Locate and identify every blood parasite.
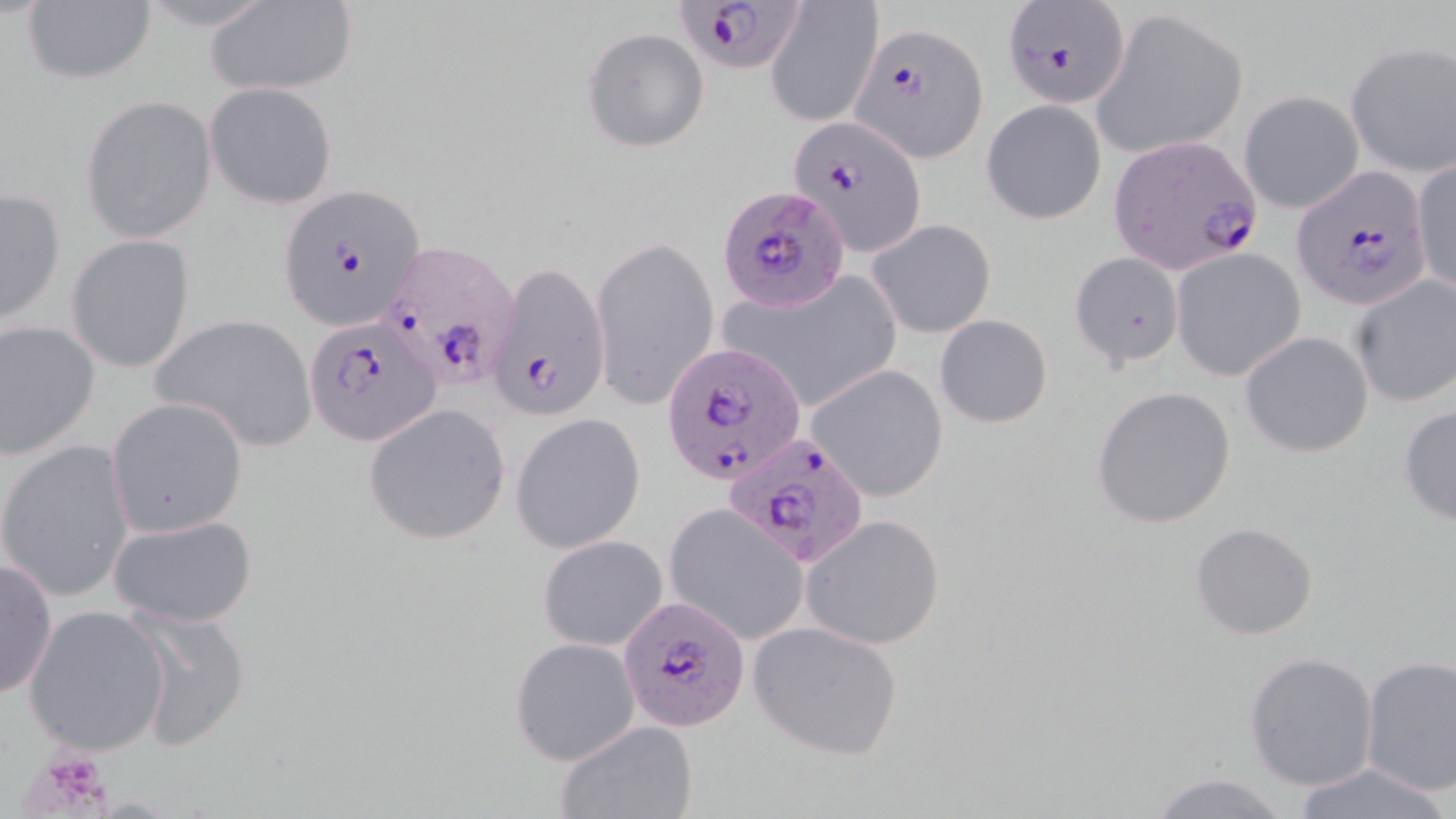
Approximate bounding boxes as (x1, y1, x2, y2) in pixels.
Plasmodium falciparum-infected red blood cells: (677, 0, 804, 75), (1003, 3, 1129, 107), (852, 23, 988, 160), (787, 114, 925, 258), (1106, 137, 1262, 274), (1295, 168, 1431, 309), (278, 185, 426, 331), (718, 185, 850, 312), (376, 239, 517, 391), (488, 257, 611, 424), (305, 316, 441, 447), (662, 340, 811, 485), (722, 433, 868, 568), (616, 595, 751, 732).
No Plasmodium ovale, Plasmodium malariae, Plasmodium vivax, Babesia divergens, or Trypanosoma brucei observed.

Summary:
  - Platelet locations: (21, 745, 117, 817)
  - Uninfected red blood cell locations: (765, 1, 882, 128), (18, 2, 158, 87), (203, 2, 358, 97), (1090, 7, 1247, 158), (583, 26, 711, 152), (1343, 41, 1455, 176), (206, 82, 339, 208), (1238, 89, 1364, 214), (81, 93, 218, 244), (980, 99, 1107, 225), (1410, 157, 1456, 300), (1, 186, 66, 325), (868, 218, 996, 339), (67, 234, 196, 374), (589, 234, 721, 411), (1171, 248, 1306, 382), (1069, 252, 1186, 370), (719, 272, 901, 417), (1350, 276, 1456, 408), (149, 314, 317, 453), (934, 314, 1053, 427), (0, 319, 100, 461), (1239, 331, 1373, 459), (806, 363, 951, 503), (1092, 385, 1238, 528), (106, 397, 248, 538), (364, 403, 511, 545), (1397, 403, 1456, 528), (510, 414, 646, 555), (1, 439, 134, 602), (664, 506, 808, 644), (107, 511, 260, 630), (800, 513, 947, 651), (1191, 522, 1318, 641), (537, 535, 669, 651), (0, 556, 57, 701), (23, 605, 171, 755), (125, 605, 253, 752), (748, 619, 906, 761), (510, 637, 640, 766), (1244, 650, 1380, 790), (1360, 655, 1456, 794), (554, 719, 699, 818), (1289, 760, 1452, 819), (1146, 771, 1292, 819)
  - Slide-level diagnosis: Plasmodium falciparum
  - Stain: May-Grünwald-Giemsa
  - Magnification: 1000x
  - Image size: 1456×819 pixels
  - Preparation: thin blood smear
  - Field of view: single
  - Modality: light microscopy